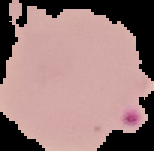
Summary:
  - Image size: 154×151 pixels
  - Image type: segmented cell region on a black background
  - Malaria status: parasitized
  - Preparation: thin blood film